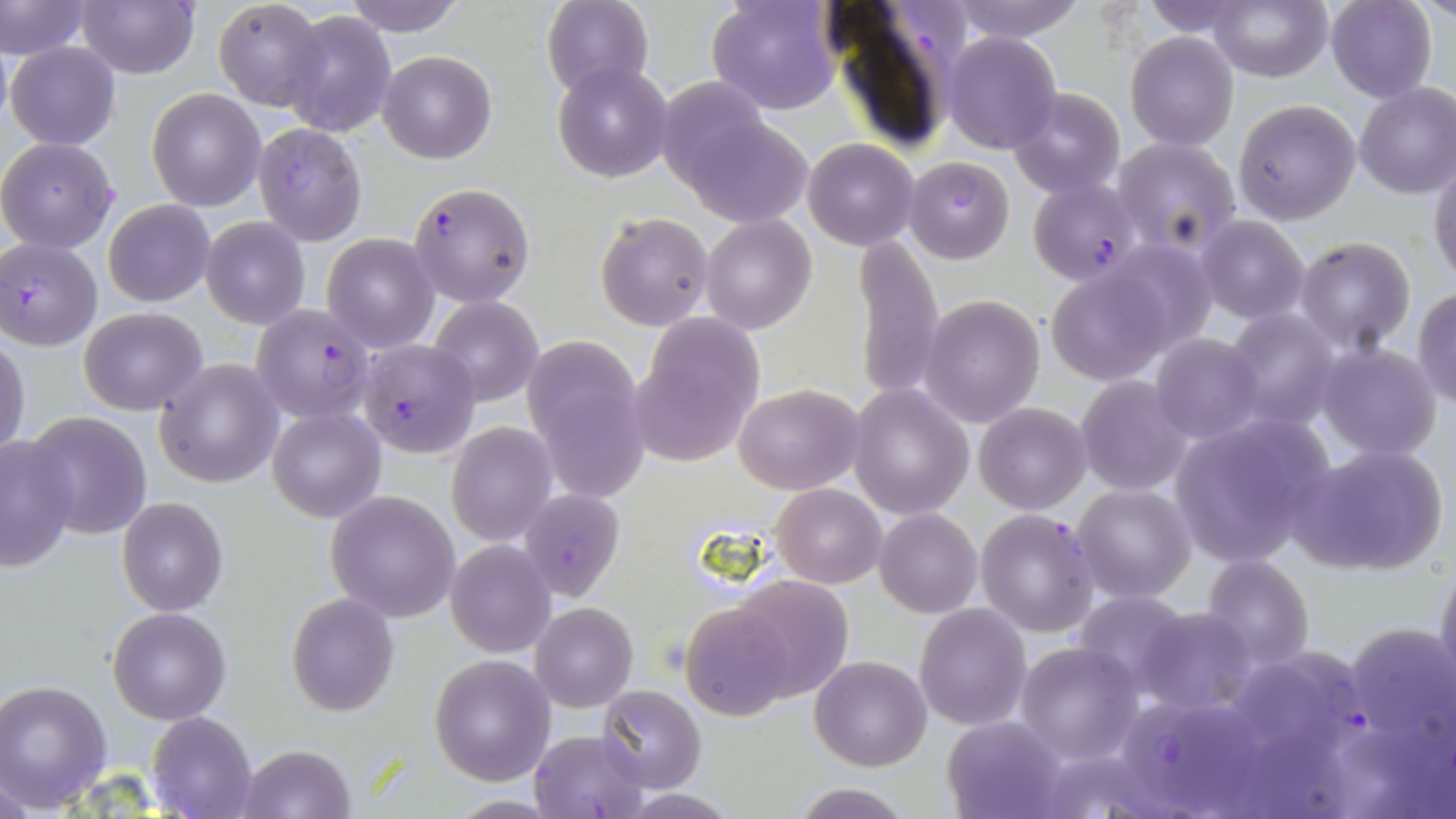
{
  "slide_level_diagnosis": "Plasmodium falciparum",
  "preparation": "thin blood film",
  "stain": "May-Grünwald-Giemsa",
  "uninfected_red_blood_cell_locations": "approximate bounding boxes as (x1, y1, x2, y2) in pixels: (1, 0, 89, 62), (75, 0, 201, 79), (340, 0, 468, 36), (542, 0, 653, 97), (707, 0, 841, 115), (947, 0, 1088, 44), (1140, 0, 1252, 40), (1208, 0, 1331, 83), (1325, 0, 1436, 102), (1421, 0, 1454, 25), (212, 1, 325, 109), (279, 10, 396, 137), (942, 31, 1062, 154), (1125, 31, 1240, 149), (6, 41, 121, 149), (377, 50, 496, 163), (553, 64, 672, 184), (656, 76, 775, 192), (1353, 82, 1456, 199), (1008, 87, 1125, 198), (147, 89, 265, 211), (1233, 99, 1363, 226), (674, 109, 813, 228), (1112, 137, 1241, 255), (0, 138, 119, 253), (804, 138, 920, 251), (904, 157, 1014, 263), (1430, 159, 1456, 285), (104, 199, 214, 306), (594, 212, 712, 331), (701, 215, 816, 335), (1196, 215, 1310, 323), (201, 217, 310, 328), (322, 233, 439, 352), (852, 233, 944, 402), (1294, 237, 1417, 354), (1045, 268, 1172, 384), (1413, 288, 1456, 407), (920, 294, 1045, 429), (428, 297, 543, 406), (78, 307, 208, 414), (1225, 308, 1341, 430), (631, 317, 766, 465), (1150, 333, 1265, 443), (1, 336, 29, 458), (523, 342, 651, 499), (1315, 342, 1442, 460), (156, 359, 283, 487), (1076, 376, 1194, 496), (848, 383, 974, 520), (733, 384, 863, 494), (974, 401, 1091, 514), (267, 407, 385, 523), (24, 411, 153, 538), (1168, 414, 1336, 571), (447, 422, 555, 546), (0, 436, 78, 572), (1291, 444, 1449, 578), (772, 483, 886, 587), (1072, 484, 1196, 601), (519, 486, 624, 602), (326, 491, 460, 623), (117, 496, 229, 618), (874, 507, 983, 618), (446, 541, 556, 657), (1201, 554, 1314, 671), (1434, 558, 1456, 698), (729, 574, 852, 700), (1071, 590, 1192, 697), (286, 593, 399, 716), (531, 603, 637, 712), (682, 603, 797, 721), (915, 604, 1032, 732), (108, 606, 232, 725), (1134, 607, 1258, 714), (1346, 620, 1456, 762), (1016, 641, 1142, 764), (429, 655, 556, 785), (809, 656, 931, 771), (1, 679, 113, 811), (597, 684, 707, 791), (148, 711, 256, 819), (942, 716, 1066, 819), (531, 728, 651, 818), (237, 744, 356, 819), (789, 783, 914, 818), (445, 795, 566, 817)",
  "magnification": "1000x",
  "modality": "light microscopy",
  "image_size": "1456×819 pixels",
  "plasmodium_falciparum_infected_red_blood_cell_locations": "approximate bounding boxes as (x1, y1, x2, y2) in pixels: (253, 123, 369, 246), (1028, 178, 1141, 286), (408, 182, 535, 308), (0, 238, 102, 350), (250, 302, 377, 424), (358, 339, 480, 457), (976, 509, 1100, 638), (1271, 645, 1371, 756), (1124, 703, 1233, 812)",
  "field_of_view": "single"
}